Assess this cell for malaria.
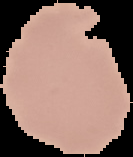
It is uninfected.

Image is 133×157 pixels. Cell region segmented out of the field of view; the surrounding area is masked to black. From a thin blood smear.